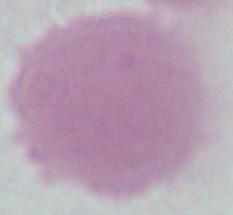

Summary:
  - Modality: micrograph
  - Identification: red blood cell
  - Magnification: 1000x